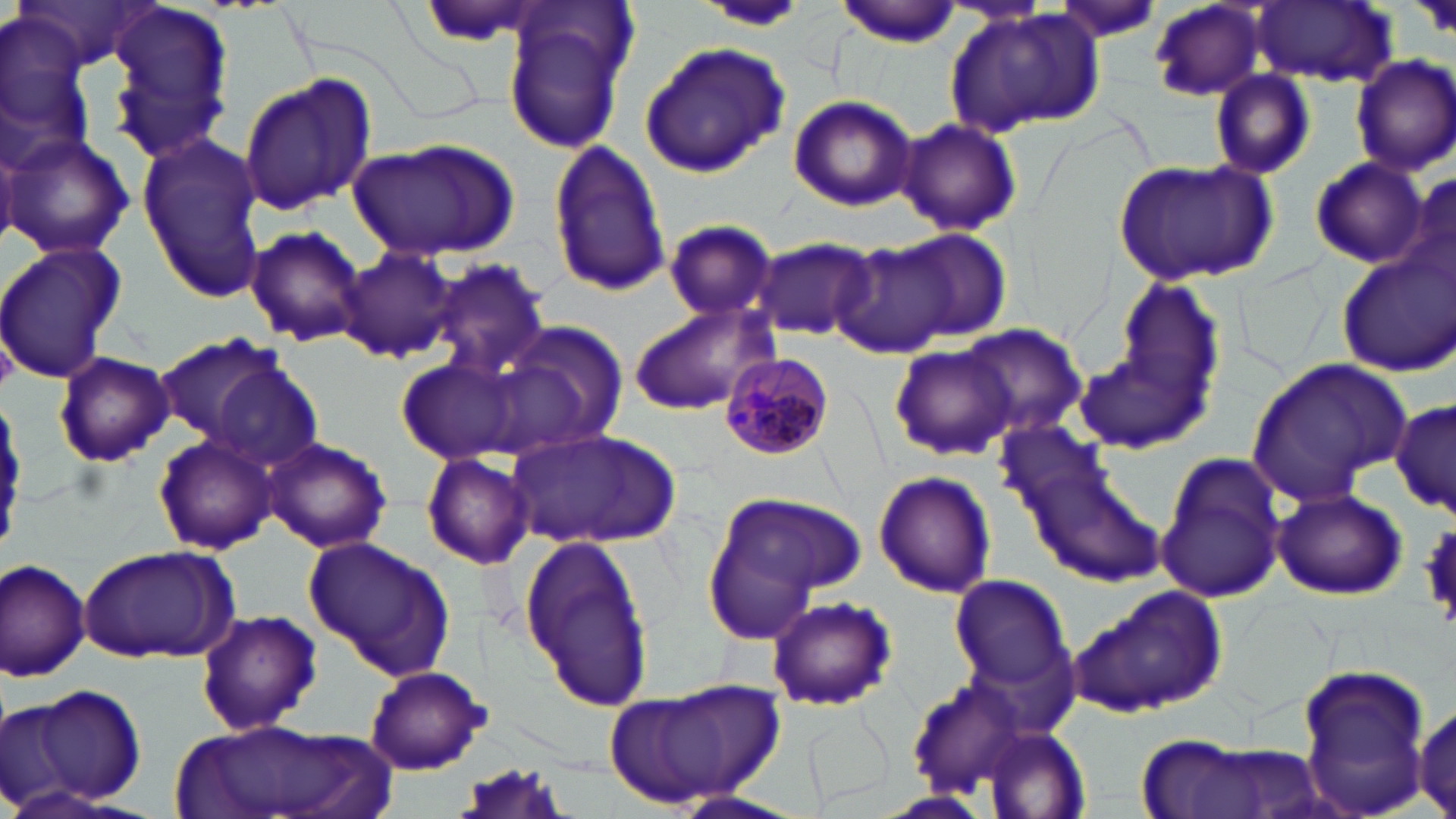
Summary:
  - Coordinate format: approximate bounding boxes as [x1, y1, x2, y2] in pixels
  - Plasmodium malariae-infected red blood cell locations: [717, 353, 831, 462]
  - Uninfected red blood cell locations: [834, 1, 963, 47], [1252, 1, 1394, 86], [501, 2, 632, 156], [1055, 2, 1165, 42], [1149, 2, 1270, 103], [0, 3, 95, 179], [699, 4, 813, 33], [101, 5, 232, 162], [942, 6, 1103, 141], [638, 39, 790, 177], [1351, 55, 1456, 175], [1210, 69, 1316, 180], [238, 74, 376, 215], [787, 95, 918, 212], [897, 117, 1021, 238], [2, 133, 135, 260], [137, 136, 264, 296], [347, 138, 520, 262], [547, 138, 669, 296], [1309, 156, 1429, 269], [1111, 158, 1277, 287], [1403, 173, 1456, 291], [663, 219, 779, 324], [243, 225, 368, 347], [893, 227, 1011, 344], [753, 236, 875, 342], [0, 240, 127, 384], [832, 240, 958, 359], [1333, 243, 1456, 376], [334, 245, 459, 364], [429, 259, 550, 382], [1116, 281, 1225, 413], [626, 303, 777, 416], [491, 320, 628, 457], [954, 322, 1088, 442], [154, 333, 288, 443], [1073, 335, 1214, 459], [893, 345, 1015, 459], [52, 352, 173, 466], [396, 356, 525, 464], [1244, 358, 1411, 508], [208, 362, 323, 472], [1389, 396, 1455, 518], [508, 428, 681, 551], [153, 433, 278, 555], [262, 437, 392, 553], [1015, 442, 1168, 590], [422, 451, 536, 569], [1153, 453, 1286, 602], [873, 469, 996, 598], [701, 488, 860, 640], [1272, 488, 1407, 600], [1421, 523, 1456, 626], [516, 530, 658, 716], [302, 535, 456, 681], [79, 545, 229, 664], [0, 555, 94, 684], [950, 575, 1071, 690], [1074, 587, 1227, 719], [766, 595, 896, 712], [194, 609, 323, 737], [365, 666, 489, 774], [1290, 666, 1437, 819], [905, 675, 1034, 795], [618, 677, 786, 808], [20, 682, 149, 808], [3, 699, 79, 814], [1413, 700, 1455, 817], [797, 709, 892, 810], [180, 718, 384, 819], [981, 729, 1090, 816], [1129, 737, 1313, 819]
  - Slide-level diagnosis: Plasmodium malariae
  - Modality: optical microscopy
  - Magnification: 1000x
  - Field of view: one of a larger specimen
  - Image size: 1456×819 pixels
  - Stain: May-Grünwald-Giemsa
  - Preparation: thin blood film